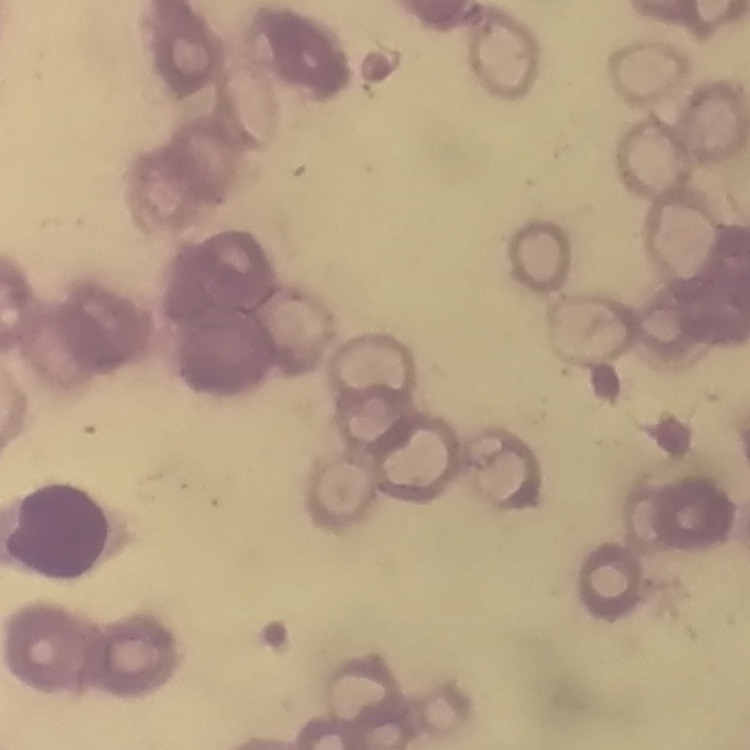
The red blood cells exhibit rouleaux formation. Stained with either Field's or Giemsa. Thin peripheral smear. Square crop of a larger photomicrograph.